Assess for parasitized red blood cells.
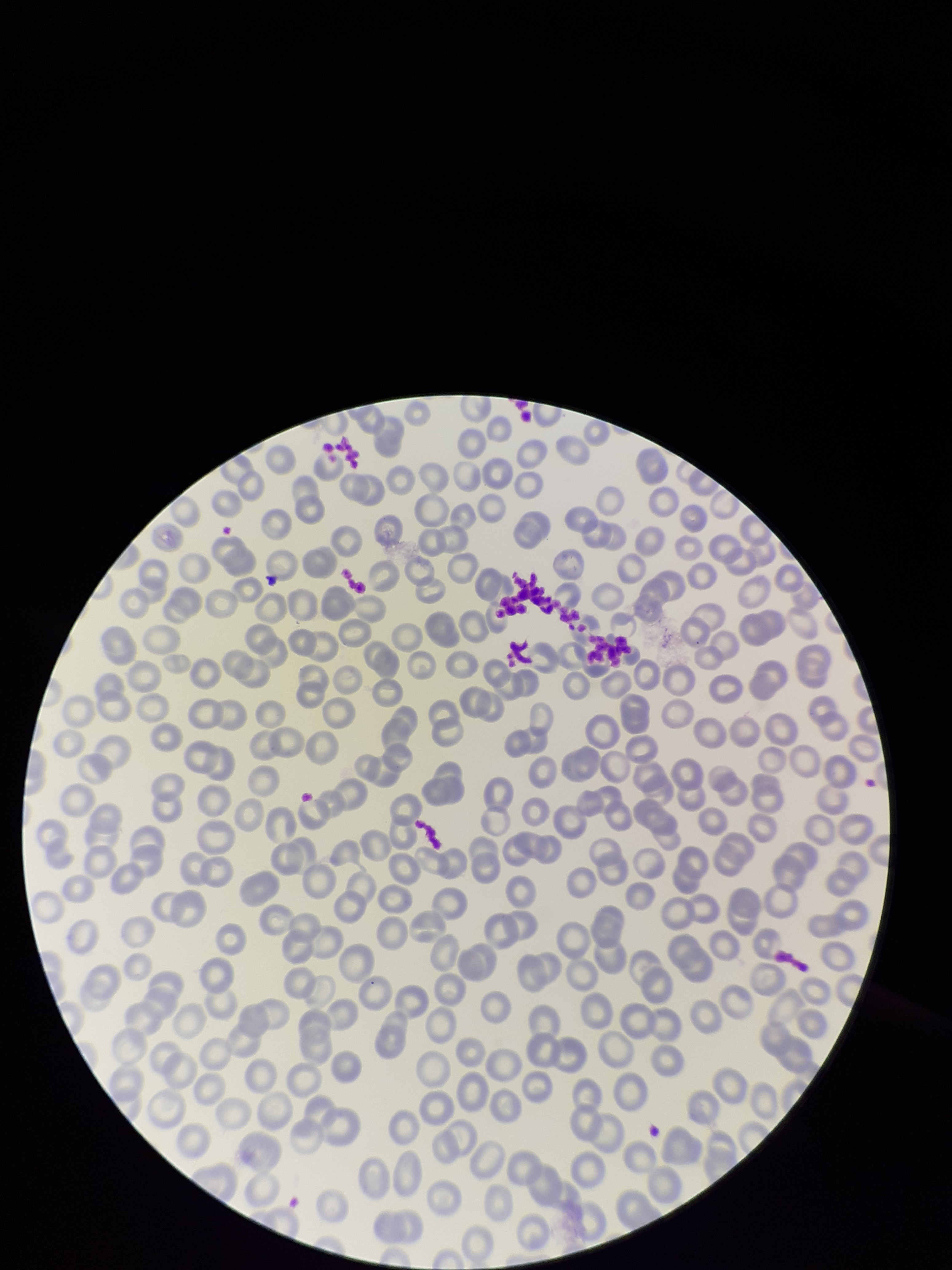
None seen.

Summary:
  - Parasitized red blood cell count: 0
  - Field of view: one from this slide
  - Red blood cell count: 225
  - Preparation: thin
  - Stain: Giemsa
  - Patient malaria status: negative
  - Image size: 952×1270 pixels
  - Capture: smartphone photograph through the microscope eyepiece